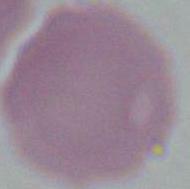

An erythrocyte is seen. Captured at 1000x magnification. Photomicrograph.